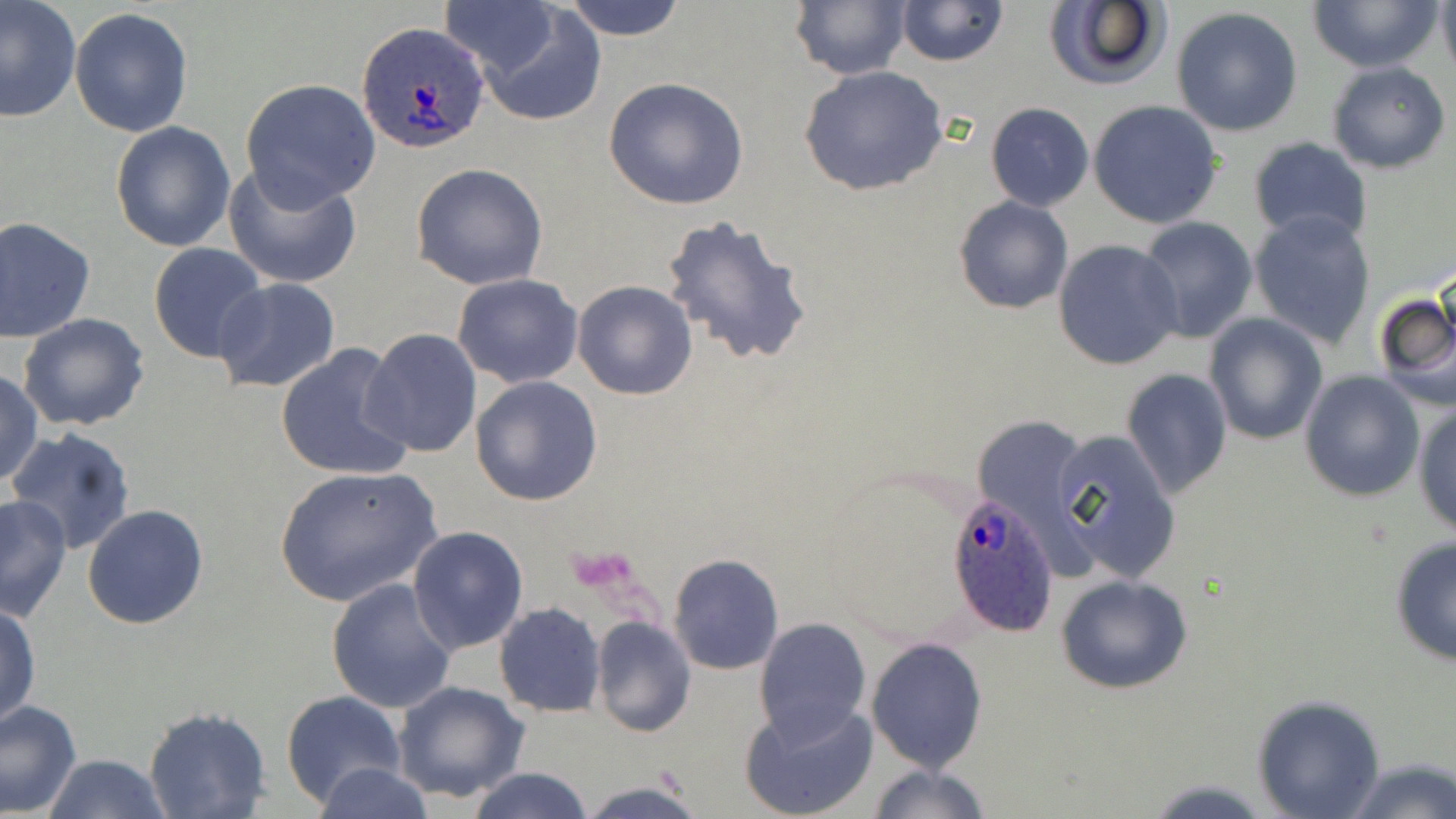

Summary:
  - Coordinate format: approximate bounding boxes as (x1,y1)-(x2,y2) corner pairs in pixels
  - Plasmodium ovale-infected red blood cell locations: (357,21)-(490,151), (947,494)-(1059,637)
  - Uninfected red blood cell locations: (0,0)-(81,122), (560,0)-(688,42), (894,0)-(1009,67), (1305,0)-(1442,73), (1437,0)-(1456,83), (790,1)-(909,80), (441,2)-(562,76), (1042,2)-(1170,90), (71,7)-(194,138), (473,7)-(608,127), (1171,7)-(1305,136), (1327,61)-(1451,173), (799,66)-(949,196), (240,78)-(383,207), (603,78)-(750,210), (1088,101)-(1223,229), (986,102)-(1093,210), (110,120)-(238,252), (1247,138)-(1373,245), (411,163)-(548,290), (224,165)-(360,289), (952,196)-(1073,315), (1250,210)-(1377,348), (660,212)-(814,368), (0,216)-(97,342), (1133,217)-(1258,342), (1052,238)-(1183,371), (148,241)-(267,362), (452,273)-(583,388), (211,278)-(341,393), (573,279)-(697,400), (1374,287)-(1456,413), (17,313)-(150,431), (1203,315)-(1326,445), (361,328)-(483,459), (276,342)-(413,481), (1122,367)-(1232,499), (0,370)-(44,486), (1299,371)-(1424,501), (470,375)-(603,507), (1413,401)-(1456,538), (6,428)-(136,555), (1049,428)-(1181,584), (273,466)-(442,607), (0,498)-(71,621), (82,504)-(209,630), (407,525)-(528,654), (1388,535)-(1456,667), (668,552)-(784,675), (1056,572)-(1194,695), (326,577)-(458,714), (0,603)-(40,732), (495,603)-(606,717), (590,616)-(696,737), (753,616)-(872,742), (866,636)-(988,772), (392,680)-(530,804), (281,691)-(405,809), (1250,694)-(1386,818), (740,697)-(878,819), (0,699)-(83,818), (143,707)-(272,819), (42,753)-(171,819), (1342,756)-(1456,819), (313,762)-(435,819), (865,762)-(991,819), (465,767)-(596,819), (1144,779)-(1273,816), (573,782)-(707,818)
  - Platelet locations: (568,546)-(638,595)
  - Slide-level diagnosis: Plasmodium ovale
  - Field of view: one of a larger specimen
  - Magnification: 1000x
  - Modality: light microscopy
  - Image size: 1456×819 pixels
  - Stain: May-Grünwald-Giemsa
  - Preparation: thin blood film